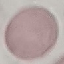

result: no malaria parasites detected
image_type: cell patch, automatically extracted from a larger field of view and resized to 64 × 64 pixels
capture: smartphone camera at the microscope eyepiece
stain: Giemsa
preparation: thin blood film